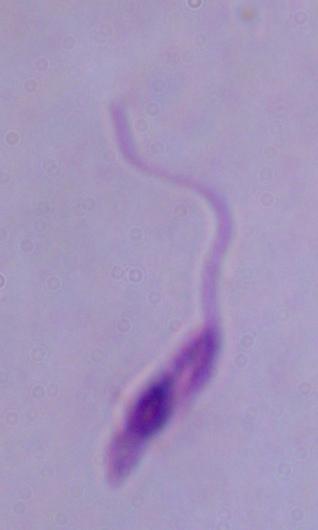
Summary:
  - Magnification: 1000x
  - Identification: Leishmania
  - Modality: micrograph